Describe the morphology of the erythrocytes.
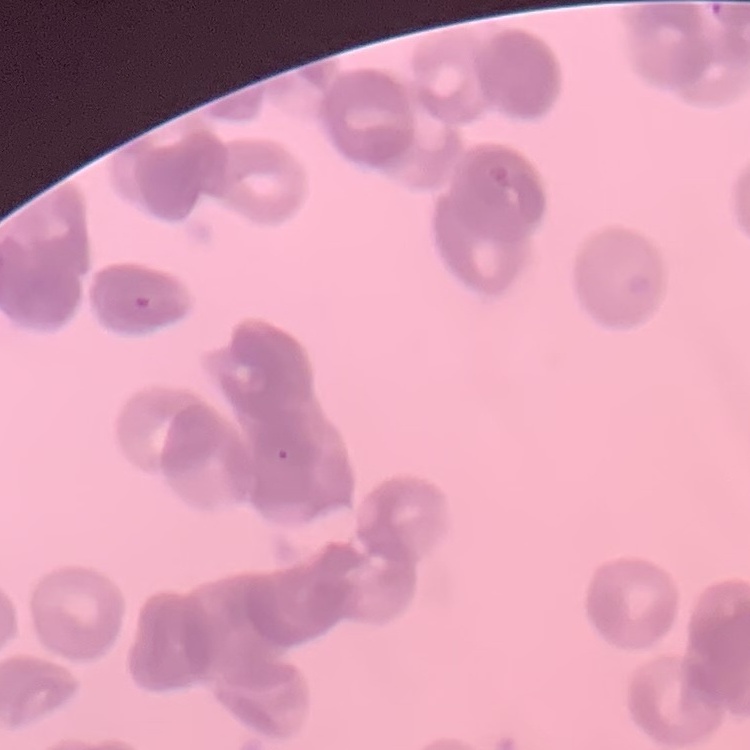

Rouleaux formation.

Field's or Giemsa stain. Square crop of a larger photomicrograph. Thin peripheral smear.